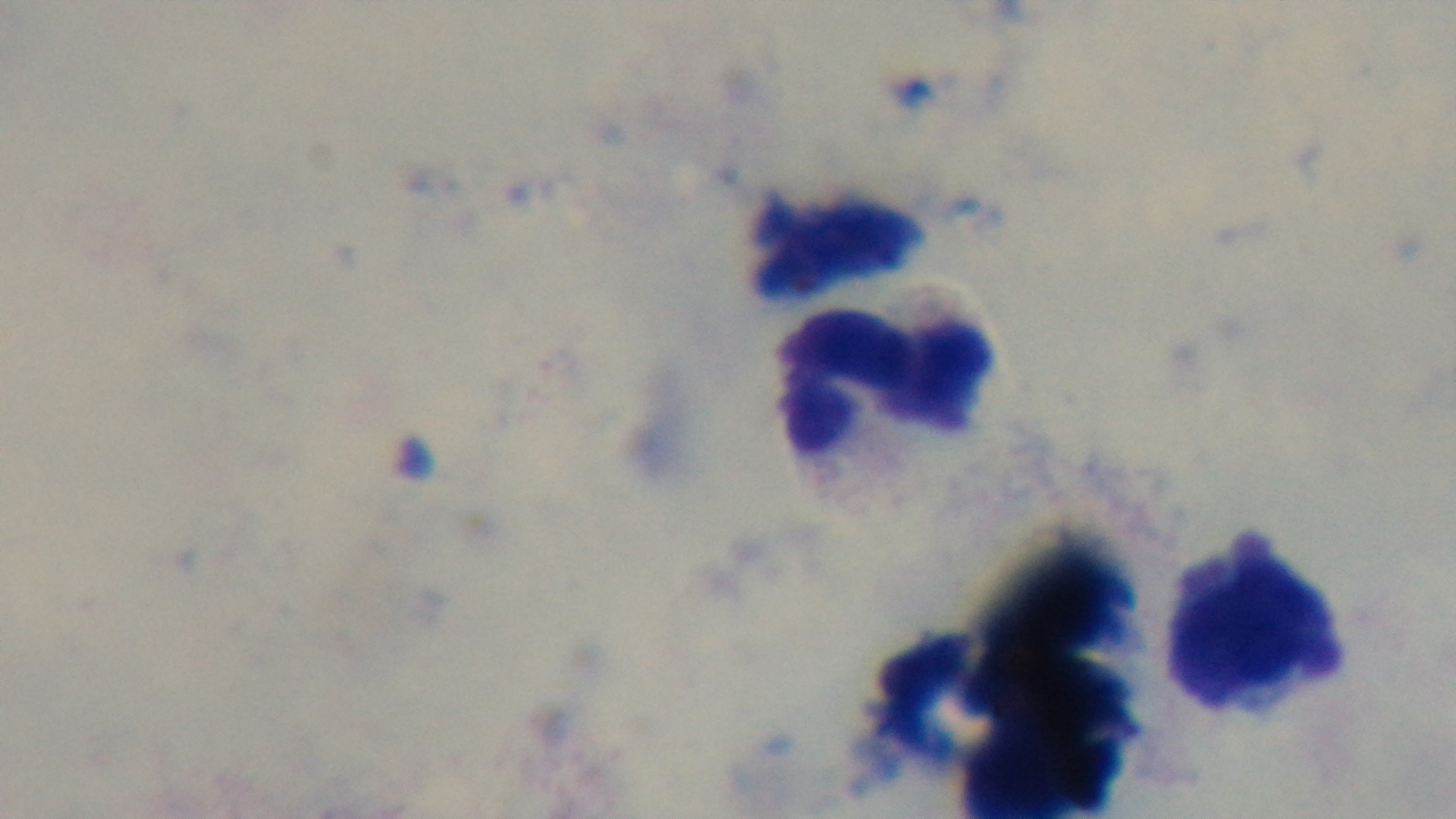

objective = 100x oil immersion
capture = mounted 4K digital camera
malaria status = uninfected
stain = Giemsa
modality = light microscopy
field of view = single
preparation = thick smear